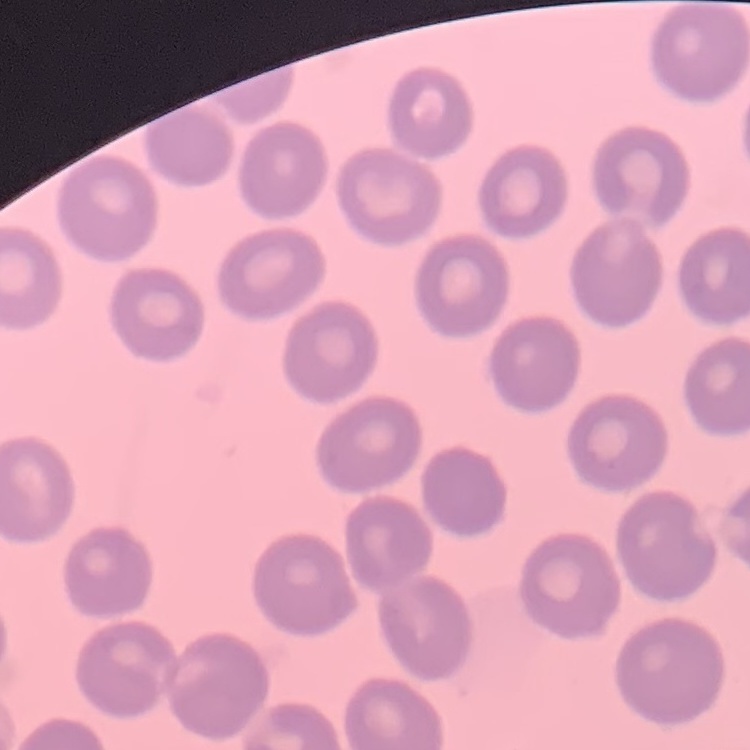
erythrocyte_morphology: no rouleaux formation
image_type: square crop of a larger photomicrograph
stain: Field's or Giemsa
preparation: thin blood smear